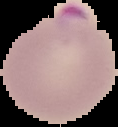

image type = segmented cell region with the area outside set to black
malaria status = parasitized
image size = 118×127 pixels
preparation = thin blood film